Describe the morphology of the erythrocytes.
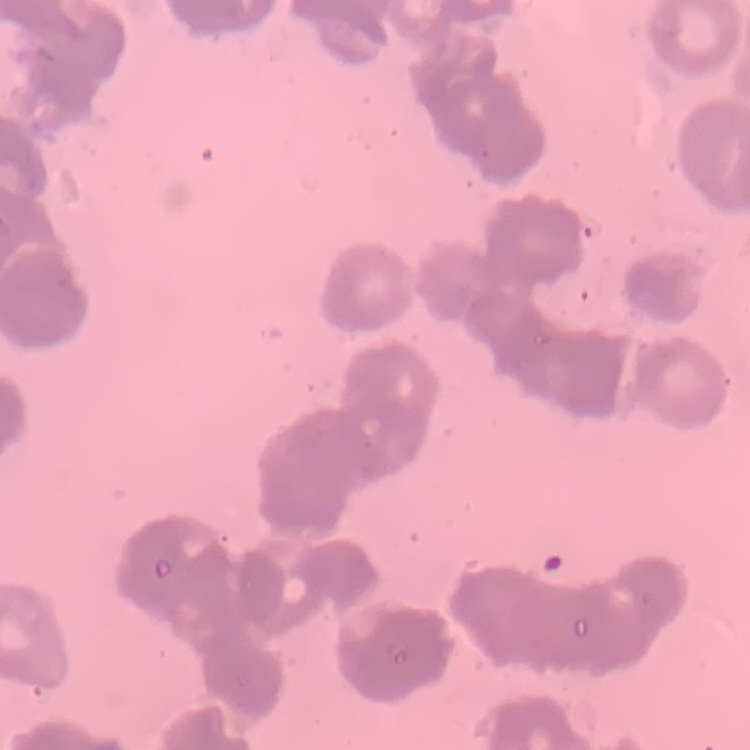
They show rouleaux formation.

Field's or Giemsa stain. Thin peripheral smear. Square crop of a larger photomicrograph.